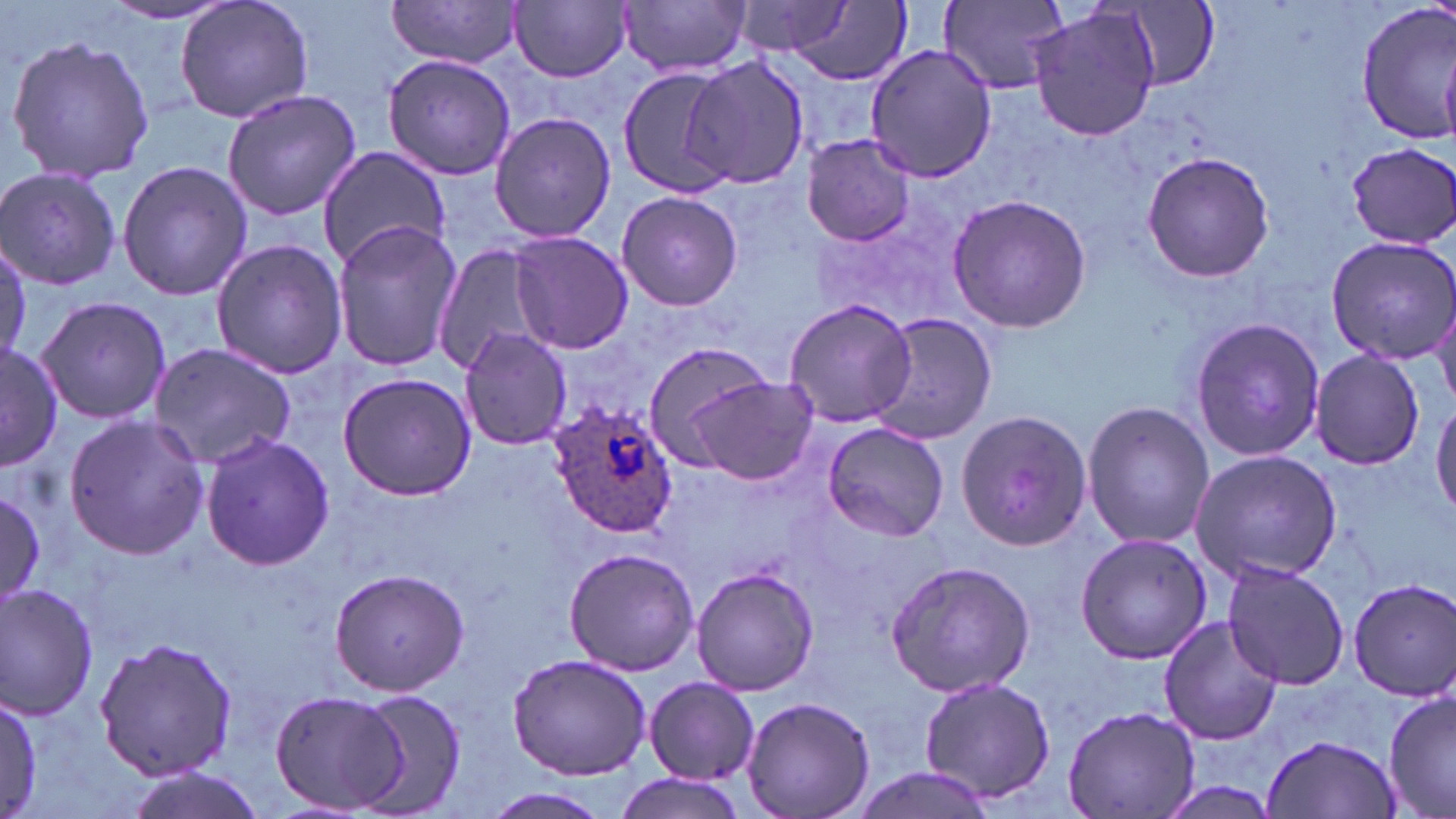
{
  "plasmodium_ovale_infected_red_blood_cell_locations": "approximate bounding boxes as (x1,y1)-(x2,y2) corner pairs in pixels: (549,399)-(679,542)",
  "slide_level_diagnosis": "Plasmodium ovale",
  "field_of_view": "single",
  "stain": "May-Grünwald-Giemsa",
  "uninfected_red_blood_cell_locations": "approximate bounding boxes as (x1,y1)-(x2,y2) corner pairs in pixels: (176,0)-(312,125), (386,0)-(525,68), (510,0)-(632,82), (619,0)-(751,78), (939,0)-(1068,93), (733,1)-(856,56), (98,2)-(242,25), (782,2)-(909,86), (1354,2)-(1456,142), (1124,3)-(1217,89), (1028,5)-(1162,142), (5,35)-(158,184), (865,42)-(998,182), (381,54)-(516,181), (615,57)-(740,200), (685,58)-(809,190), (221,90)-(362,220), (488,112)-(619,243), (801,135)-(915,245), (1347,140)-(1456,244), (319,145)-(451,269), (1141,151)-(1275,284), (117,160)-(254,301), (0,167)-(121,290), (614,190)-(743,312), (946,194)-(1094,332), (331,221)-(462,372), (507,231)-(633,354), (0,233)-(29,369), (1325,234)-(1456,364), (209,239)-(348,379), (434,245)-(552,378), (35,295)-(170,425), (1432,297)-(1456,410), (781,298)-(920,429), (868,312)-(996,446), (1188,314)-(1324,464), (459,327)-(573,450), (149,341)-(299,470), (0,342)-(63,468), (638,342)-(786,469), (1311,350)-(1424,469), (337,370)-(479,500), (690,377)-(824,485), (1431,396)-(1456,521), (1080,400)-(1214,550), (956,409)-(1097,554), (63,414)-(208,559), (822,421)-(949,542), (198,431)-(334,572), (1189,450)-(1341,582), (1,490)-(45,601), (1075,533)-(1211,663), (561,548)-(700,677), (884,559)-(1036,698), (1220,562)-(1351,690), (690,564)-(819,698), (326,567)-(470,695), (1345,576)-(1456,701), (1,581)-(100,721), (1158,616)-(1282,746), (93,637)-(239,780), (508,652)-(651,780), (917,673)-(1058,806), (644,676)-(761,783), (1382,684)-(1456,819), (267,687)-(411,815), (346,687)-(470,814), (2,689)-(44,813), (741,696)-(875,819), (1061,704)-(1202,819), (1262,729)-(1401,817), (848,766)-(997,819), (120,767)-(265,819), (610,775)-(747,819), (475,789)-(613,819)",
  "image_size": "1456×819 pixels",
  "preparation": "thin blood smear",
  "magnification": "1000x",
  "modality": "optical microscopy"
}